Assess the morphology of the red blood cells.
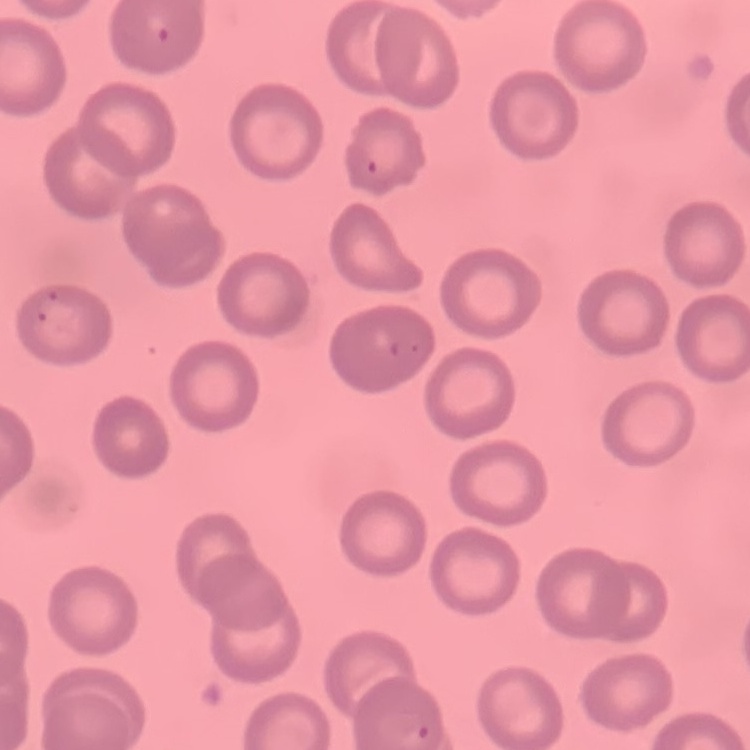

No rouleaux formation.

Field's or Giemsa stain. Thin peripheral smear. Square crop of a larger photomicrograph.